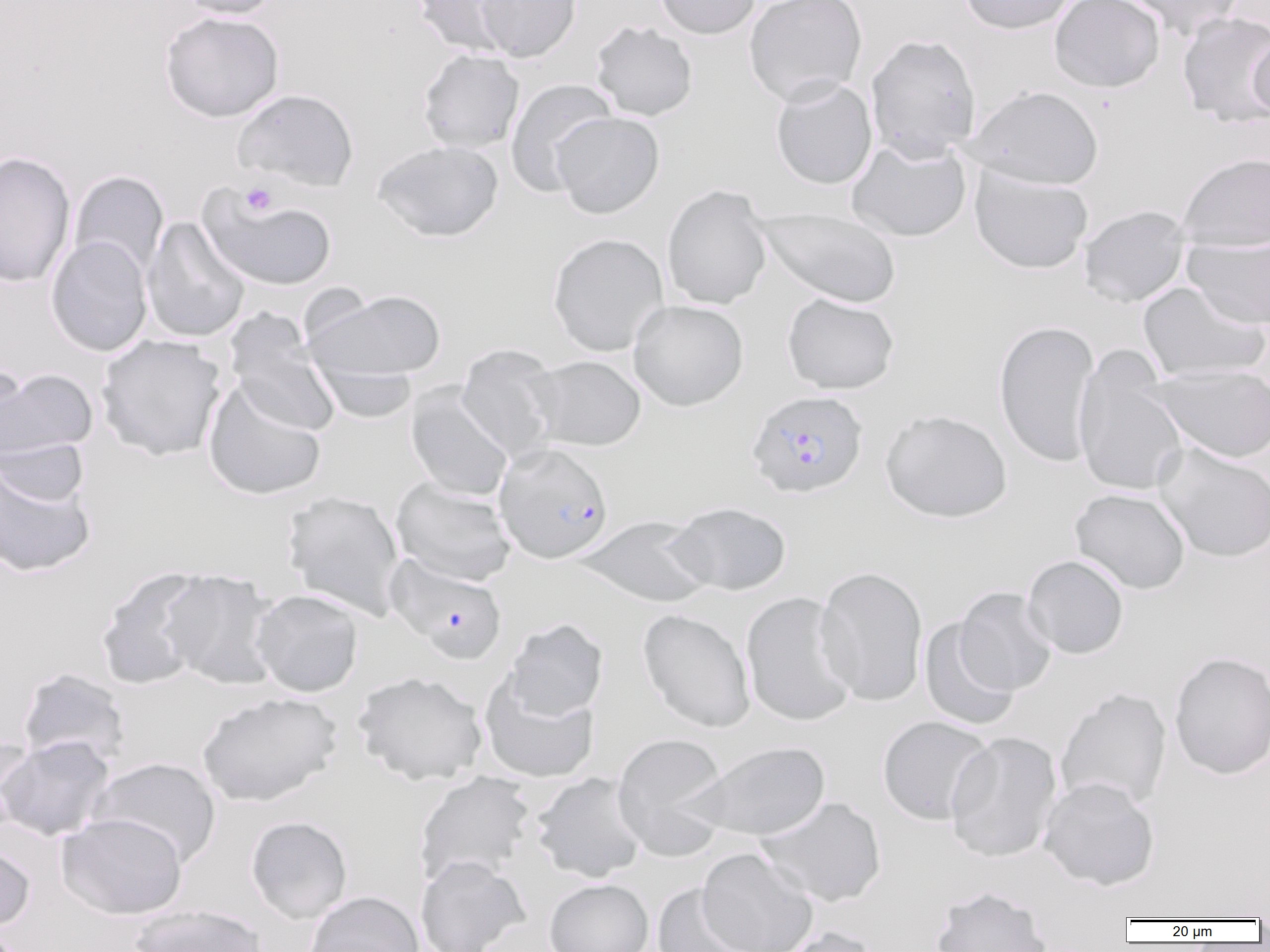
Summary:
  - Coordinate format: approximate bounding boxes as (x1,y1)-(x2,y2) corner pairs in pixels
  - Platelet locations: (240,182)-(277,216)
  - Uninfected red blood cell locations: (174,0)-(282,19), (412,0)-(519,55), (475,0)-(581,62), (654,0)-(762,39), (744,0)-(868,106), (958,0)-(1078,34), (1050,0)-(1165,92), (1118,0)-(1247,39), (160,11)-(285,122), (1177,11)-(1270,127), (591,20)-(698,121), (1249,33)-(1270,120), (865,34)-(982,162), (417,49)-(525,154), (770,77)-(878,189), (505,78)-(617,196), (969,85)-(1104,190), (232,87)-(359,191), (551,111)-(665,218), (846,137)-(972,243), (373,140)-(503,242), (0,151)-(77,288), (1177,152)-(1270,251), (969,166)-(1093,275), (68,170)-(169,279), (661,185)-(773,310), (197,186)-(338,292), (1078,205)-(1191,308), (756,207)-(901,308), (142,217)-(250,343), (547,232)-(669,356), (45,235)-(153,357), (1184,236)-(1270,330), (1138,280)-(1269,382), (304,288)-(447,383), (782,292)-(899,395), (628,300)-(749,411), (224,314)-(342,437), (994,319)-(1101,467), (95,333)-(228,461), (455,344)-(563,463), (1072,348)-(1189,497), (527,355)-(646,451), (312,359)-(418,423), (1145,364)-(1270,464), (1,367)-(99,467), (202,380)-(327,500), (405,385)-(514,502), (880,409)-(1012,523), (1154,443)-(1270,563), (0,450)-(97,579), (391,477)-(517,586), (1069,488)-(1190,594), (281,490)-(405,620), (667,501)-(792,596), (575,515)-(715,608), (1023,555)-(1129,659), (815,565)-(928,707), (95,566)-(215,691), (160,569)-(283,690), (954,586)-(1057,696), (251,589)-(364,697), (739,592)-(859,727), (637,608)-(756,733), (919,617)-(1020,731), (504,618)-(609,720), (1169,651)-(1270,780), (16,668)-(131,768), (353,671)-(488,785), (478,672)-(601,784), (1055,687)-(1172,811), (196,691)-(342,807), (876,716)-(995,825), (944,731)-(1063,863), (612,733)-(732,860), (0,735)-(116,842), (0,736)-(36,837), (686,740)-(831,842), (88,757)-(221,868), (413,771)-(536,887), (531,772)-(649,883), (1039,776)-(1160,891), (756,795)-(887,908), (57,812)-(187,920), (245,816)-(352,923), (0,838)-(36,932), (697,847)-(819,952), (415,854)-(531,952), (544,878)-(654,952), (650,884)-(760,952), (929,886)-(1052,952), (303,890)-(424,952), (129,904)-(268,952), (774,926)-(881,952)
  - Plasmodium falciparum-infected red blood cell locations: (746,390)-(869,499), (494,442)-(614,564), (386,555)-(508,664)
  - Slide-level diagnosis: Plasmodium falciparum
  - Magnification: 1000x
  - Modality: optical microscopy
  - Field of view: one of a larger specimen
  - Image size: 1270×952 pixels
  - Preparation: thin blood film